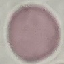

Result: negative for malaria parasites. Photographed with a smartphone camera at the microscope eyepiece. Thin blood smear. Cell patch, automatically extracted from a larger field of view and resized to 64 × 64 pixels. Giemsa stain.